Name the cell type shown.
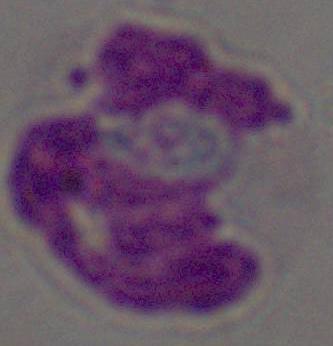

This is a leukocyte.

{
  "modality": "micrograph",
  "magnification": "1000x"
}